Describe the morphology of the red blood cells.
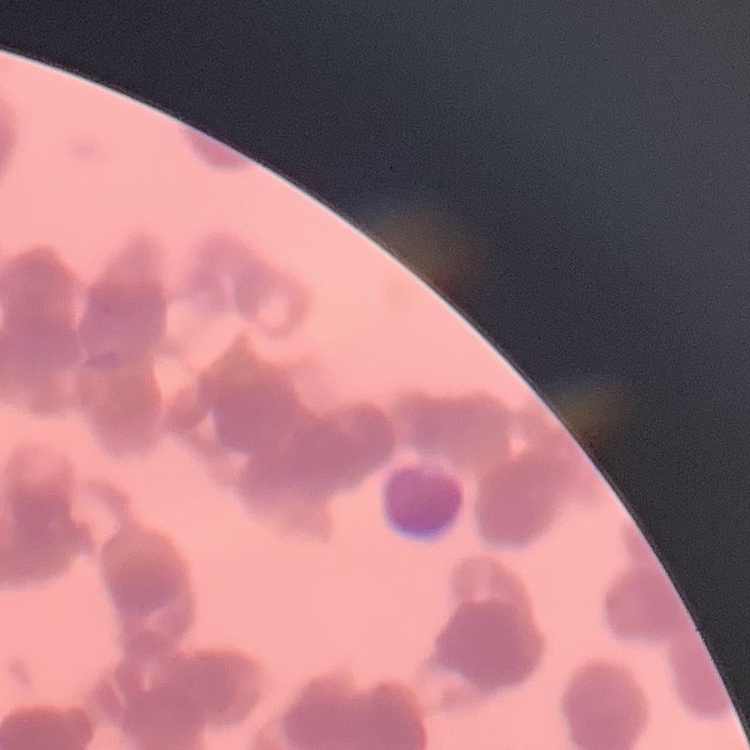

They show rouleaux formation.

Summary:
  - Stain: Field's or Giemsa
  - Preparation: thin peripheral smear
  - Image type: one tile cut from a larger photomicrograph